Assess this cell for malaria.
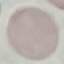
It is uninfected.

{
  "preparation": "thin blood smear",
  "capture": "smartphone camera at the microscope eyepiece",
  "image_type": "automatically extracted cell patch, resized to 64 × 64 pixels",
  "stain": "Giemsa"
}